Name the parasite shown.
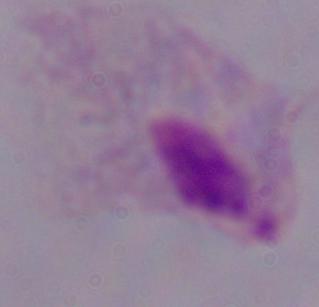

A trichomonad.

modality: micrograph
magnification: 1000x